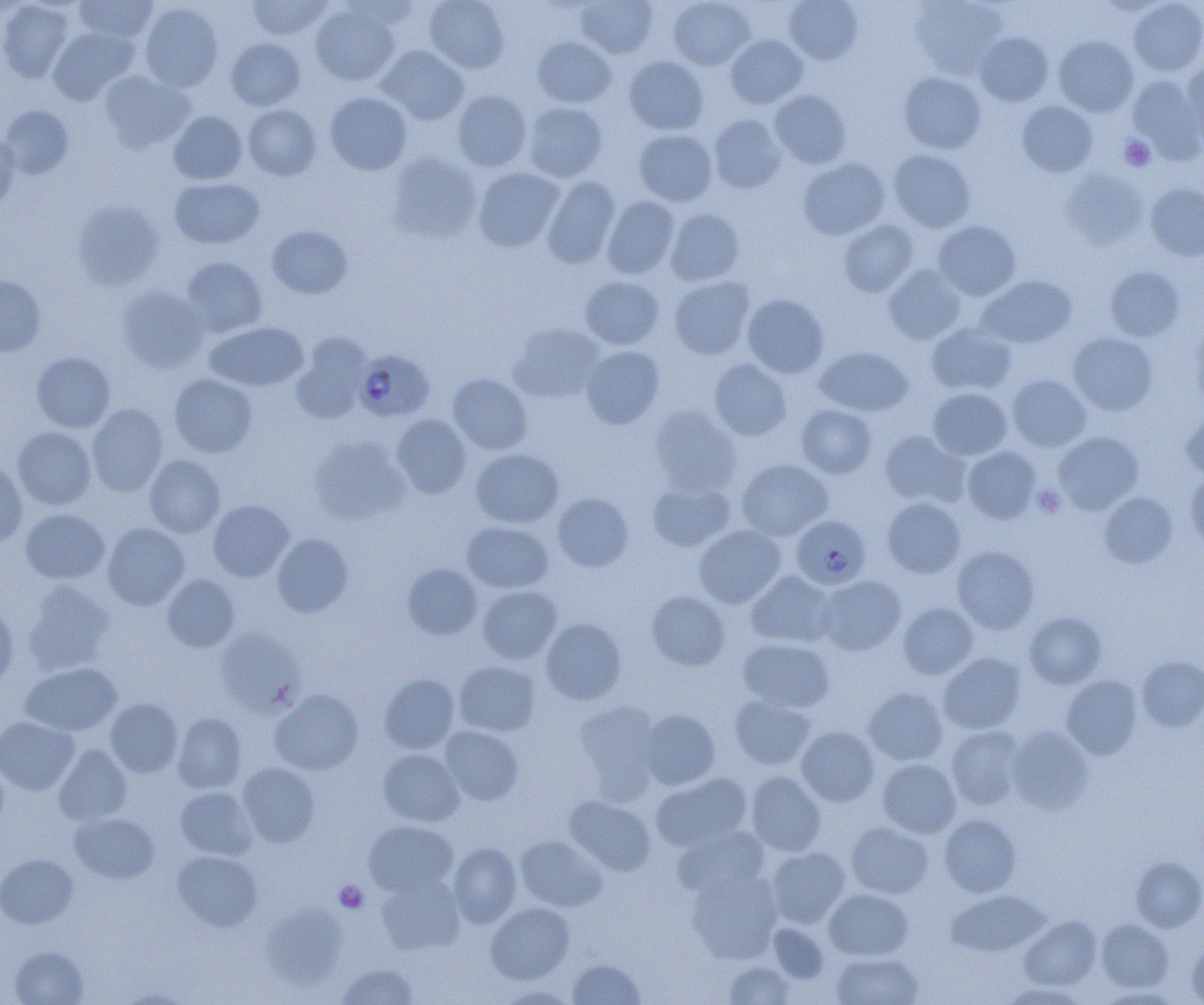

slide_level_diagnosis: Plasmodium falciparum
field_of_view: one of a larger specimen
modality: light microscopy
image_size: 1204×1005 pixels
preparation: thin blood film
uninfected_red_blood_cell_locations: 'approximate bounding boxes as (x1,y1)-(x2,y2) corner pairs in pixels: (74,0)-(158,44), (246,0)-(333,41), (424,0)-(510,74), (575,0)-(659,58), (668,0)-(756,70), (784,0)-(864,64), (911,0)-(1009,78), (1129,0)-(1204,76), (0,1)-(74,82), (138,2)-(224,92), (310,3)-(400,85), (48,27)-(139,104), (974,32)-(1054,106), (725,34)-(809,108), (1054,35)-(1139,116), (532,36)-(616,107), (226,37)-(305,110), (376,45)-(470,125), (624,55)-(709,135), (1180,61)-(1204,145), (97,70)-(194,153), (898,72)-(986,154), (1127,74)-(1203,161), (452,89)-(532,171), (769,90)-(851,169), (324,91)-(412,174), (1016,101)-(1098,177), (523,102)-(607,181), (0,104)-(75,179), (242,104)-(322,181), (168,110)-(247,184), (708,114)-(786,193), (634,129)-(717,205), (0,131)-(20,215), (889,149)-(976,232), (387,150)-(483,243), (798,158)-(890,240), (473,167)-(564,252), (1061,169)-(1148,249), (169,176)-(265,249), (541,176)-(621,268), (1145,183)-(1204,262), (602,195)-(680,279), (72,199)-(164,290), (665,208)-(745,285), (838,218)-(918,296), (933,220)-(1021,300), (266,224)-(354,300), (181,256)-(268,337), (883,264)-(967,344), (1104,266)-(1185,341), (0,274)-(46,357), (580,275)-(664,349), (978,275)-(1077,348), (668,276)-(755,359), (116,285)-(209,374), (742,294)-(829,378), (1189,317)-(1204,410), (205,322)-(308,391), (508,323)-(606,404), (926,323)-(1016,395), (1067,331)-(1158,415), (291,332)-(373,423), (581,345)-(665,430), (815,345)-(913,416), (31,351)-(115,433), (709,358)-(792,441), (169,373)-(258,458), (447,373)-(532,454), (1007,374)-(1091,451), (928,387)-(1013,460), (86,403)-(168,496), (796,404)-(878,478), (649,405)-(741,495), (1180,409)-(1204,481), (391,414)-(471,498), (11,426)-(97,510), (879,430)-(968,508), (1053,431)-(1144,514), (310,437)-(410,525), (962,445)-(1041,523), (470,448)-(563,529), (144,455)-(226,537), (736,459)-(834,540), (0,461)-(27,549), (1184,472)-(1204,553), (647,479)-(735,552), (1099,491)-(1178,568), (552,492)-(634,572), (882,497)-(966,578), (207,499)-(294,582), (20,508)-(110,584), (461,521)-(554,593), (103,522)-(189,610), (694,525)-(786,607), (271,533)-(354,617), (952,545)-(1041,633), (401,562)-(483,640), (746,570)-(837,648), (161,574)-(240,653), (816,575)-(906,656), (23,580)-(116,675), (477,585)-(562,664), (646,591)-(730,670), (0,602)-(18,688), (897,602)-(978,679), (1024,611)-(1106,689), (540,618)-(626,704), (214,628)-(304,716), (736,638)-(836,713), (938,652)-(1026,734), (1137,655)-(1204,732), (453,660)-(541,737), (20,662)-(122,737), (379,673)-(460,754), (1061,675)-(1143,760), (863,686)-(949,766), (269,689)-(364,775), (729,694)-(816,770), (105,698)-(183,777), (574,700)-(662,800), (639,709)-(720,790), (172,712)-(247,793), (0,716)-(79,795), (1007,724)-(1094,814), (945,725)-(1027,809), (440,726)-(524,805), (796,726)-(880,806), (54,743)-(132,825), (378,748)-(464,826), (877,758)-(961,837), (237,763)-(321,848), (745,771)-(827,856), (650,772)-(752,852), (175,786)-(258,860), (564,796)-(656,875), (70,812)-(159,883), (938,813)-(1022,897), (363,820)-(458,897), (845,821)-(934,898), (673,826)-(771,898), (515,835)-(607,912), (447,842)-(522,927), (765,847)-(850,927), (172,851)-(263,931), (0,854)-(78,928), (1131,857)-(1204,932), (686,868)-(782,963), (376,875)-(465,955), (824,888)-(914,961), (945,890)-(1050,957), (261,901)-(348,989), (485,902)-(575,984), (1019,916)-(1102,990), (1095,918)-(1174,993), (767,923)-(830,984), (1186,938)-(1204,1003), (9,946)-(89,1005), (831,952)-(924,1005), (567,957)-(647,1004), (723,960)-(796,1004), (335,962)-(419,1005), (998,982)-(1090,1005), (495,985)-(576,1004)'
magnification: 1000x
plasmodium_falciparum_infected_red_blood_cell_locations: 'approximate bounding boxes as (x1,y1)-(x2,y2) corner pairs in pixels: (354,349)-(435,422), (790,514)-(870,590)'
platelet_locations: 'approximate bounding boxes as (x1,y1)-(x2,y2) corner pairs in pixels: (1120,135)-(1156,172), (1033,484)-(1065,517), (334,880)-(368,912)'